Assess this cell for malaria.
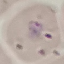

It is parasitized.

Summary:
  - Preparation: thin blood film
  - Capture: smartphone through the microscope eyepiece
  - Image type: automatically extracted cell patch, resized to 64 × 64 pixels
  - Stain: Giemsa